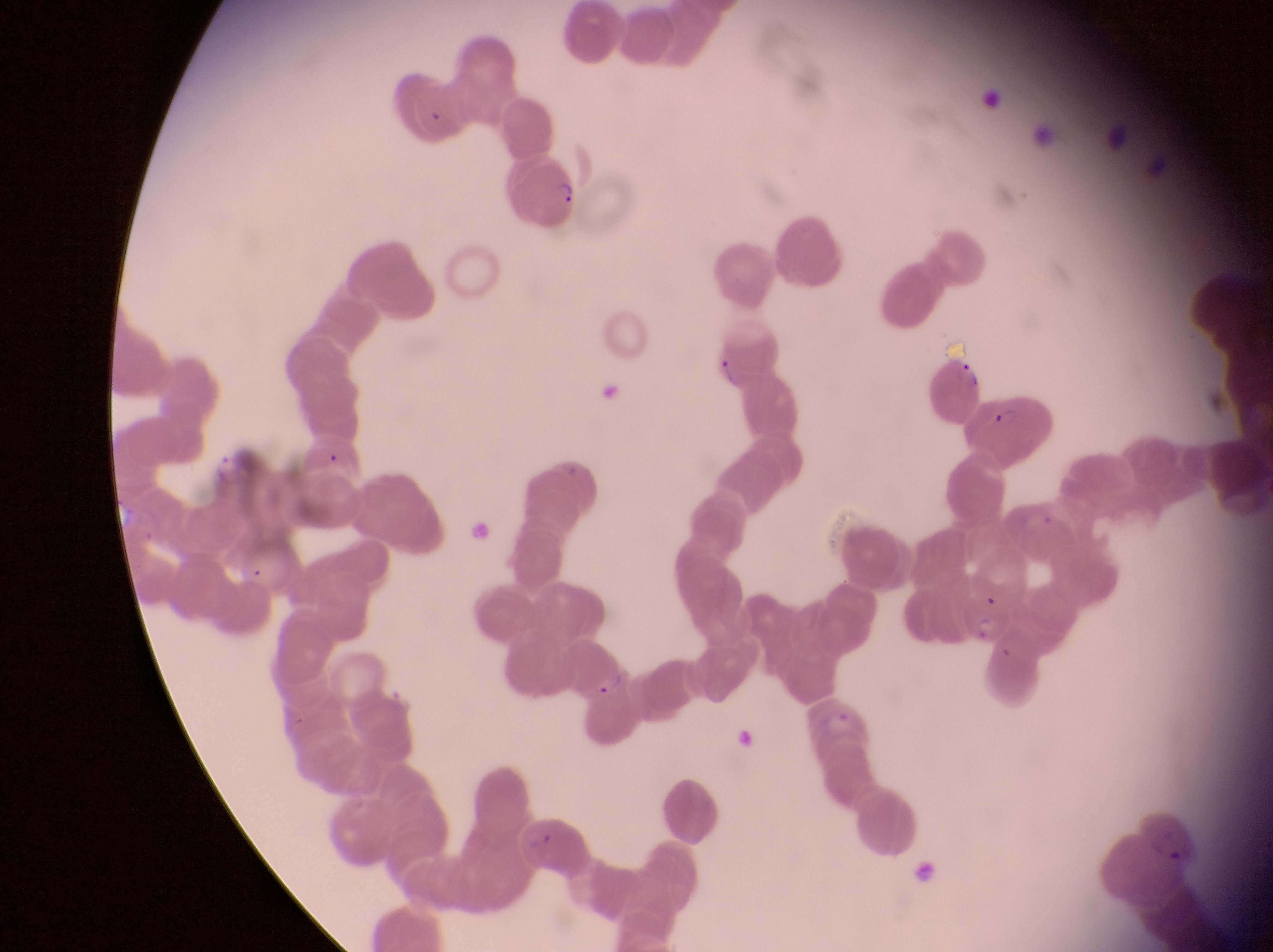
Approximate bounding boxes as left top right bottom in pixels. Trophozoite locations: 205 449 247 486. Parasitised red blood cell locations: 512 158 578 228; 928 359 991 427; 969 395 1056 467; 587 664 642 749; 801 692 871 755. Captured by a smartphone held over the eyepiece of an Olympus CX-23 microscope. Image is 1273×952 pixels. Thin blood film. Single field of view. Sample from Uganda. Magnification of 1000x.